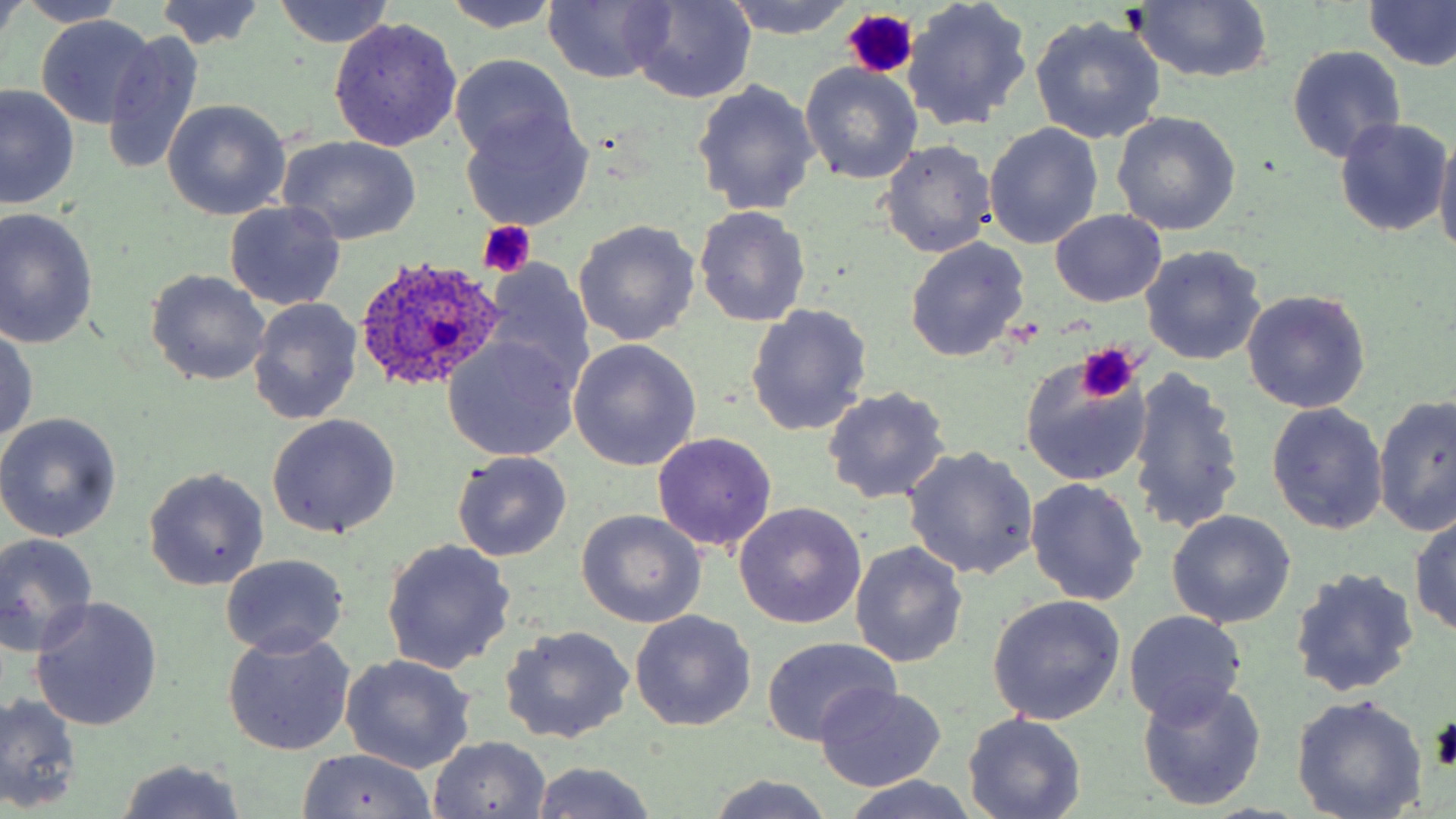
Approximate bounding boxes as (x1,y1)-(x2,y2) corner pairs in pixels. Uninfected red blood cell locations: (0,0)-(25,48), (15,0)-(134,28), (440,0)-(563,32), (623,0)-(758,105), (720,0)-(855,38), (903,0)-(1032,129), (155,1)-(268,51), (271,1)-(394,48), (1363,1)-(1456,72), (542,2)-(674,84), (1129,2)-(1274,84), (34,16)-(157,128), (1029,16)-(1166,144), (329,17)-(462,152), (103,31)-(203,175), (1287,45)-(1406,164), (449,54)-(578,167), (800,64)-(922,185), (691,81)-(819,216), (1,86)-(78,210), (162,100)-(291,219), (460,109)-(592,230), (1111,112)-(1241,235), (1335,119)-(1451,237), (984,123)-(1102,249), (1434,133)-(1456,259), (278,136)-(422,245), (879,141)-(995,257), (224,201)-(345,310), (694,205)-(810,327), (0,209)-(100,348), (1050,210)-(1168,306), (574,220)-(700,345), (906,236)-(1029,361), (1140,245)-(1265,365), (482,262)-(593,393), (145,269)-(271,385), (1241,289)-(1370,413), (248,299)-(361,426), (744,305)-(872,438), (0,323)-(39,447), (444,336)-(580,462), (567,339)-(701,470), (1019,357)-(1151,486), (1126,366)-(1245,537), (821,387)-(950,505), (1375,395)-(1455,537), (1266,403)-(1389,534), (0,413)-(123,542), (266,413)-(401,539), (652,432)-(777,551), (902,446)-(1038,580), (452,452)-(571,562), (144,467)-(269,591), (1025,477)-(1147,607), (734,503)-(867,629), (1410,508)-(1456,639), (578,509)-(707,627), (1166,510)-(1296,629), (0,533)-(98,657), (380,540)-(516,673), (850,542)-(968,667), (220,554)-(348,657), (1290,568)-(1418,695), (986,594)-(1126,724), (31,596)-(163,731), (631,611)-(754,730), (1125,611)-(1247,724), (500,626)-(633,744), (222,629)-(355,756), (761,636)-(899,747), (341,655)-(476,773), (1138,679)-(1266,812), (814,684)-(946,790), (0,693)-(81,812), (1292,696)-(1428,817), (962,712)-(1086,819), (430,736)-(551,818), (297,747)-(439,818), (114,761)-(247,817), (530,763)-(657,819), (705,774)-(836,819), (838,777)-(986,818). Platelet locations: (843,9)-(916,78), (475,222)-(535,278), (1077,342)-(1142,403). Plasmodium ovale-infected red blood cell locations: (354,257)-(504,393). Slide-level diagnosis: Plasmodium ovale. One field of a larger specimen. Image is 1456×819 pixels. May-Grünwald-Giemsa stain. Thin blood smear. Captured at 1000x magnification. Optical microscopy.